Locate every leukocyte (white blood cell).
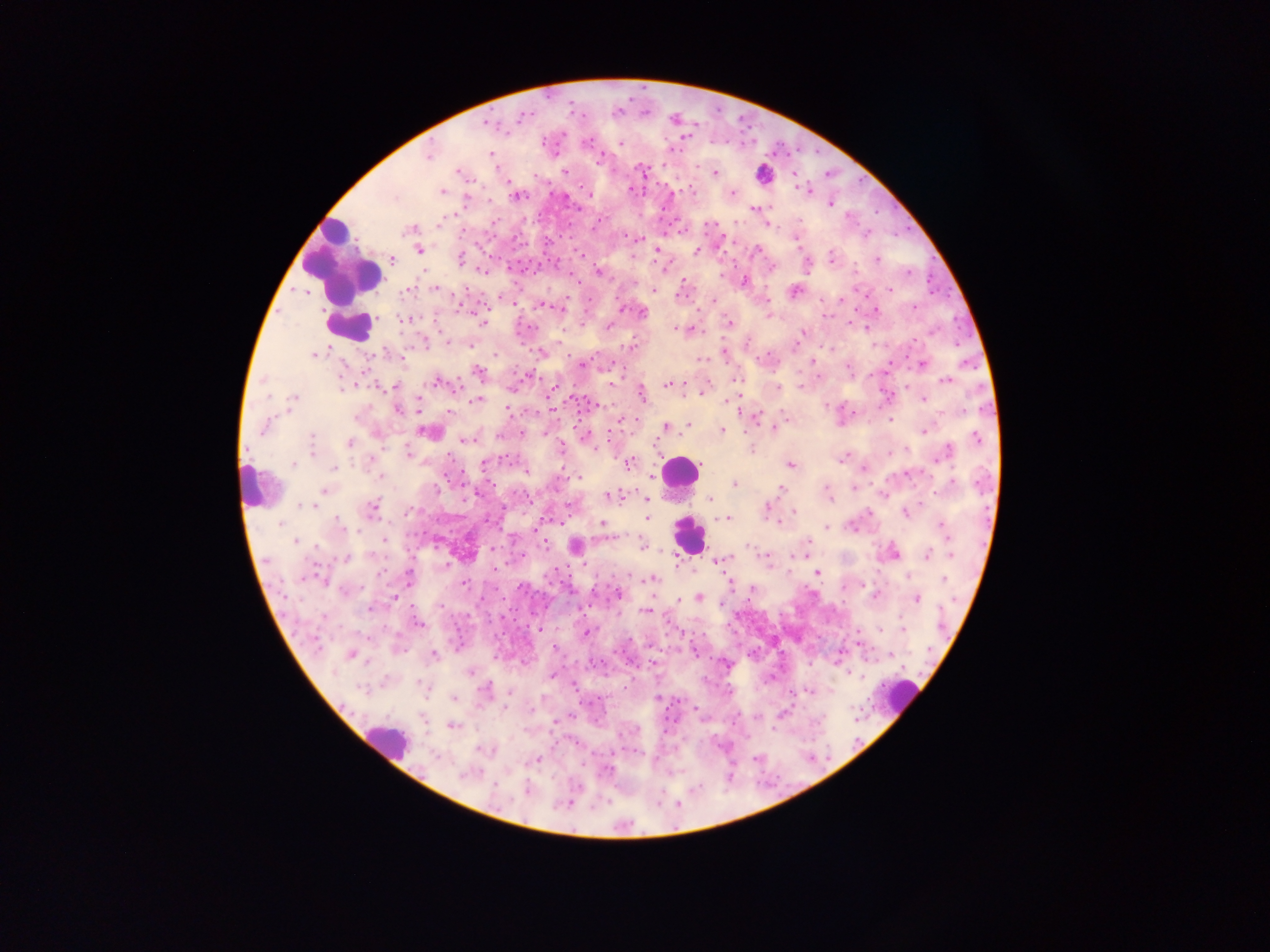
Approximate centers as [x, y] in pixels.
Leukocytes: [766, 172], [343, 261], [350, 326], [679, 470], [251, 488], [688, 536], [902, 696], [387, 740].

Plasmodium parasite locations = approximate centers as [x, y] in pixels: [521, 117], [489, 123], [685, 136], [621, 143], [490, 154], [428, 156], [600, 158], [642, 168], [565, 171], [457, 172], [715, 172], [805, 189], [631, 190], [442, 192], [589, 194], [733, 194], [516, 196], [466, 200], [831, 204], [753, 208], [409, 230], [638, 238], [419, 249], [657, 251], [695, 251], [756, 251], [581, 255], [831, 256], [392, 259], [460, 259], [877, 260], [909, 271], [599, 274], [744, 282], [435, 289], [889, 289], [407, 291], [655, 291], [794, 291], [841, 298], [545, 306], [914, 307], [876, 310], [641, 312], [405, 319], [482, 322], [729, 323], [609, 326], [678, 329], [802, 333], [446, 341], [631, 346], [725, 352], [541, 353], [314, 354], [701, 358], [812, 362], [581, 364], [921, 364], [849, 367], [478, 372], [736, 380], [946, 380], [437, 382], [667, 384], [685, 384], [394, 386], [555, 387], [778, 388], [641, 393], [293, 399], [477, 400], [923, 400], [398, 410], [754, 416], [355, 418], [621, 421], [666, 426], [687, 426], [264, 427], [773, 428], [722, 429], [923, 430], [426, 432], [544, 432], [522, 433], [499, 435], [976, 436], [311, 438], [465, 440], [350, 443], [752, 449], [310, 450], [561, 450], [408, 452], [945, 453], [841, 459], [371, 460], [484, 463], [628, 463], [293, 464], [791, 464], [334, 468], [526, 473], [578, 477], [381, 478], [734, 484], [952, 484], [438, 487], [780, 488], [325, 491], [827, 492], [611, 495], [648, 499], [711, 500], [302, 505], [310, 506], [373, 508], [767, 508], [793, 511], [868, 512], [906, 514], [647, 518], [728, 518], [338, 522], [601, 523], [281, 524], [851, 526], [942, 526], [827, 527], [384, 540], [296, 541], [807, 542], [545, 545], [575, 545], [643, 546], [492, 550], [893, 553], [927, 554], [952, 556], [346, 557], [722, 560], [816, 572], [409, 576], [651, 579], [944, 579], [465, 584], [346, 590], [618, 594], [395, 596], [875, 596], [698, 597], [916, 598], [680, 600], [722, 604], [369, 608], [646, 611], [323, 617], [418, 623], [903, 628], [879, 629], [586, 633], [351, 654], [434, 654], [470, 672], [552, 675], [485, 688], [454, 698], [656, 698], [453, 726], [536, 760], [466, 776], [494, 785], [527, 791]
image size = 1270×952 pixels
field of view = single
country = Ghana
preparation = thick blood film
capture = mobile-phone photograph through a microscope